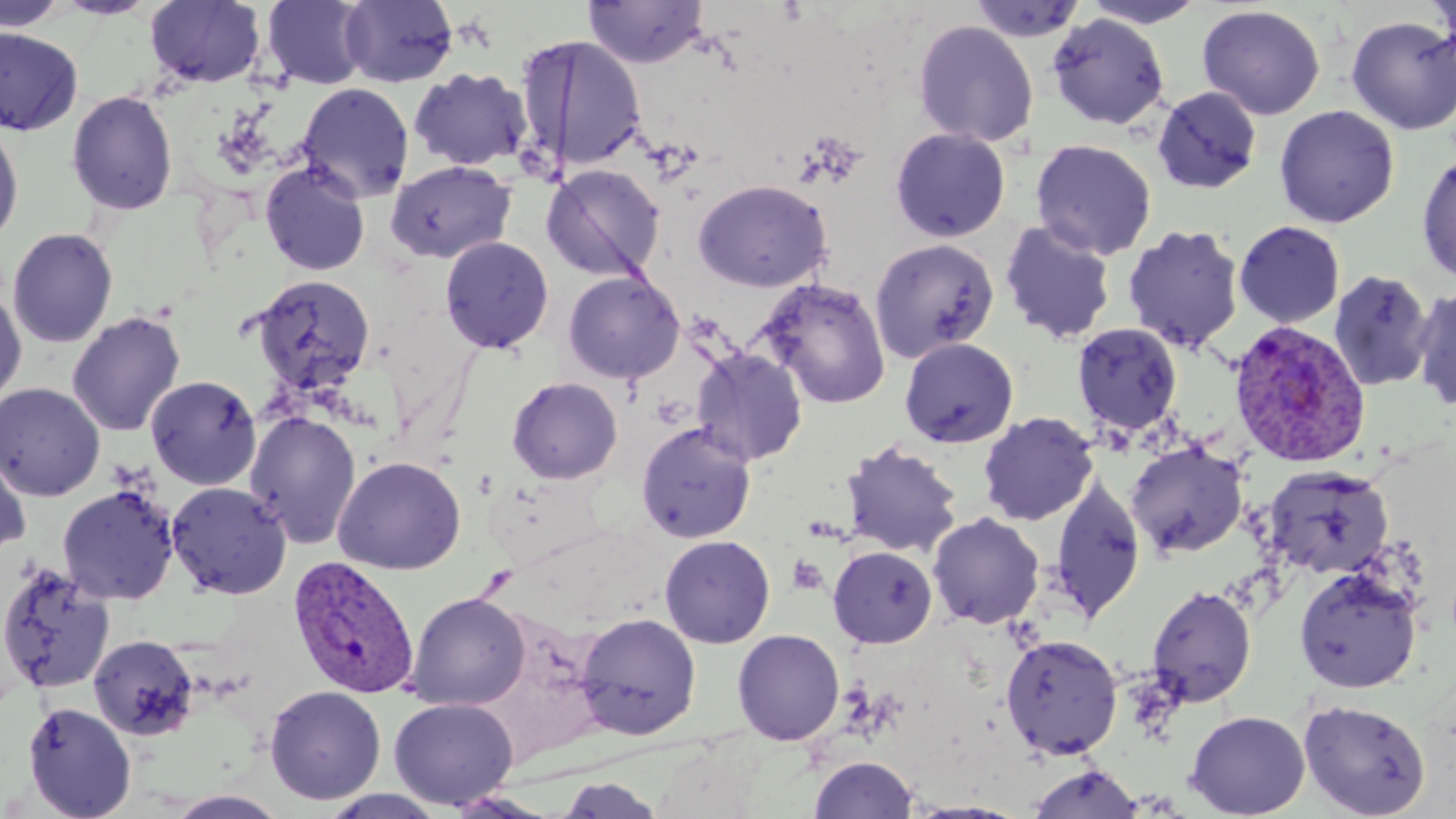

Approximate bounding boxes as [x1, y1, x2, y2] in pixels. Plasmodium vivax-infected red blood cell locations: [1228, 320, 1372, 469], [288, 555, 421, 699]. Uninfected red blood cell locations: [0, 0, 70, 32], [261, 0, 371, 90], [339, 0, 459, 88], [1079, 0, 1210, 28], [144, 1, 267, 89], [583, 1, 708, 69], [967, 1, 1088, 43], [1197, 5, 1326, 120], [1047, 13, 1170, 130], [1345, 15, 1456, 135], [912, 19, 1039, 148], [0, 27, 84, 135], [514, 34, 648, 173], [408, 67, 533, 172], [296, 82, 415, 203], [1151, 85, 1262, 195], [66, 90, 178, 215], [1274, 105, 1400, 228], [0, 121, 24, 248], [890, 127, 1011, 243], [1030, 139, 1157, 260], [1416, 152, 1456, 285], [259, 159, 370, 277], [385, 159, 517, 264], [540, 163, 666, 282], [693, 179, 832, 292], [999, 218, 1118, 345], [1233, 220, 1346, 328], [1122, 223, 1245, 354], [6, 227, 118, 349], [439, 236, 554, 354], [870, 238, 1000, 362], [562, 270, 685, 385], [1328, 270, 1435, 393], [249, 274, 376, 396], [756, 277, 891, 409], [1411, 283, 1456, 413], [0, 285, 27, 407], [67, 310, 186, 437], [1071, 322, 1183, 437], [899, 337, 1019, 448], [690, 346, 808, 465], [145, 374, 262, 491], [507, 376, 622, 485], [0, 382, 106, 501], [244, 410, 362, 549], [978, 411, 1099, 526], [636, 421, 757, 543], [840, 439, 964, 558], [1125, 440, 1249, 559], [0, 448, 31, 560], [332, 455, 467, 575], [1263, 466, 1395, 580], [1049, 474, 1146, 623], [166, 480, 292, 600], [57, 484, 180, 605], [927, 512, 1045, 629], [659, 534, 775, 649], [827, 545, 937, 649], [0, 561, 116, 695], [1294, 565, 1423, 694], [1147, 584, 1257, 708], [404, 592, 531, 710], [575, 612, 701, 740], [732, 629, 845, 746], [88, 633, 200, 741], [999, 633, 1123, 761], [264, 685, 386, 804], [388, 696, 519, 809], [1298, 698, 1431, 818], [22, 700, 137, 819], [1185, 710, 1311, 818], [653, 740, 766, 819], [808, 755, 918, 818], [1027, 762, 1145, 819], [554, 777, 668, 817], [318, 789, 451, 819], [165, 790, 292, 818], [444, 790, 560, 818], [903, 800, 1032, 818]. Platelet locations: [787, 555, 829, 596]. Slide-level diagnosis: Plasmodium vivax. Thin blood smear. Image is 1456×819 pixels. Single field of view. 1000x magnification. May-Grünwald-Giemsa-stained preparation. Optical microscopy.